Classify this cell by malaria status.
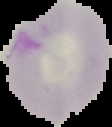

It is parasitized.

The area outside the segmented cell region is set to black. From a thin blood film. Image is 112×127 pixels.